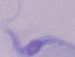

{
  "identification": "trypanosome",
  "modality": "micrograph",
  "magnification": "1000x"
}